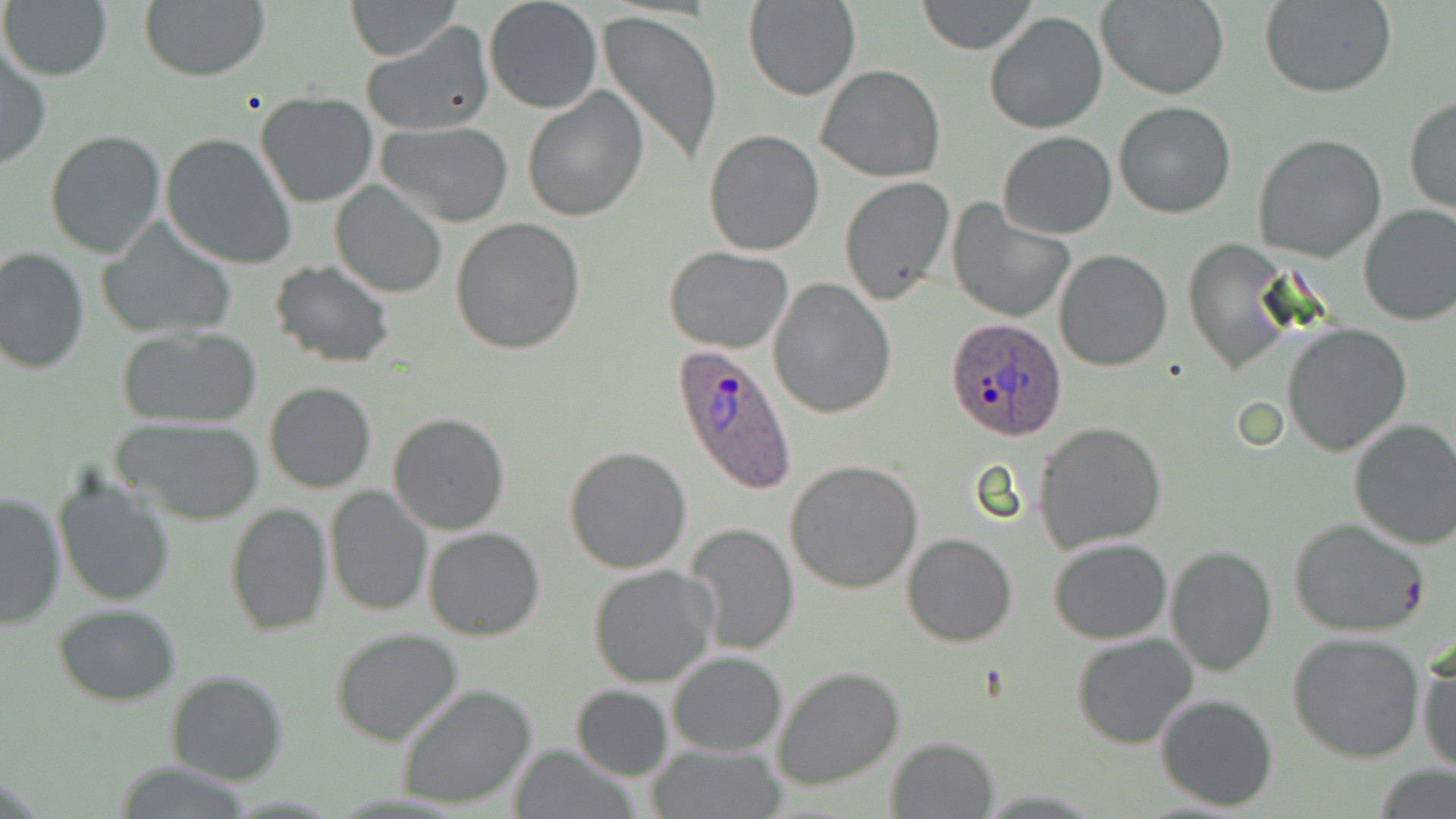

Approximate bounding boxes as (x1, y1, x2, y2) in pixels. Plasmodium ovale-infected red blood cell locations: (944, 319, 1069, 441), (672, 343, 798, 495). Uninfected red blood cell locations: (346, 0, 462, 61), (483, 0, 602, 115), (743, 0, 859, 101), (916, 0, 1037, 54), (1097, 0, 1229, 100), (138, 1, 270, 82), (1261, 1, 1398, 99), (2, 2, 111, 81), (597, 9, 724, 170), (984, 11, 1107, 135), (361, 24, 496, 137), (0, 47, 51, 171), (815, 64, 948, 182), (520, 85, 648, 224), (255, 91, 379, 208), (1403, 96, 1456, 216), (1114, 102, 1237, 219), (375, 122, 517, 227), (706, 128, 823, 254), (44, 130, 166, 260), (160, 132, 297, 269), (997, 132, 1117, 240), (1252, 132, 1387, 262), (839, 177, 956, 306), (330, 182, 447, 298), (947, 200, 1074, 324), (1358, 203, 1456, 327), (451, 219, 587, 356), (99, 222, 237, 342), (1185, 238, 1295, 373), (664, 245, 794, 353), (0, 247, 91, 374), (1053, 248, 1175, 372), (270, 261, 396, 368), (767, 276, 894, 418), (1281, 323, 1413, 456), (116, 325, 264, 429), (264, 380, 377, 494), (388, 413, 510, 535), (115, 417, 264, 526), (1348, 417, 1456, 551), (1033, 422, 1168, 552), (564, 447, 693, 574), (786, 459, 922, 594), (52, 475, 175, 607), (325, 486, 431, 616), (0, 490, 66, 632), (224, 502, 333, 636), (1289, 517, 1431, 639), (685, 523, 800, 655), (422, 526, 545, 640), (901, 532, 1018, 646), (1047, 538, 1173, 643), (1164, 545, 1278, 677), (587, 564, 719, 688), (53, 604, 182, 705), (331, 627, 464, 746), (1287, 630, 1427, 762), (1071, 631, 1198, 749), (1417, 645, 1456, 776), (666, 651, 786, 757), (772, 665, 905, 791), (165, 669, 288, 786), (397, 682, 537, 810), (569, 684, 675, 781), (1154, 693, 1279, 811), (884, 736, 1000, 819), (506, 742, 637, 818), (648, 742, 783, 818), (112, 762, 254, 818), (1373, 763, 1453, 817). Slide-level diagnosis: Plasmodium ovale. May-Grünwald-Giemsa stain. Image is 1456×819 pixels. Light microscopy. Thin blood film. Single field of view. 1000x magnification.